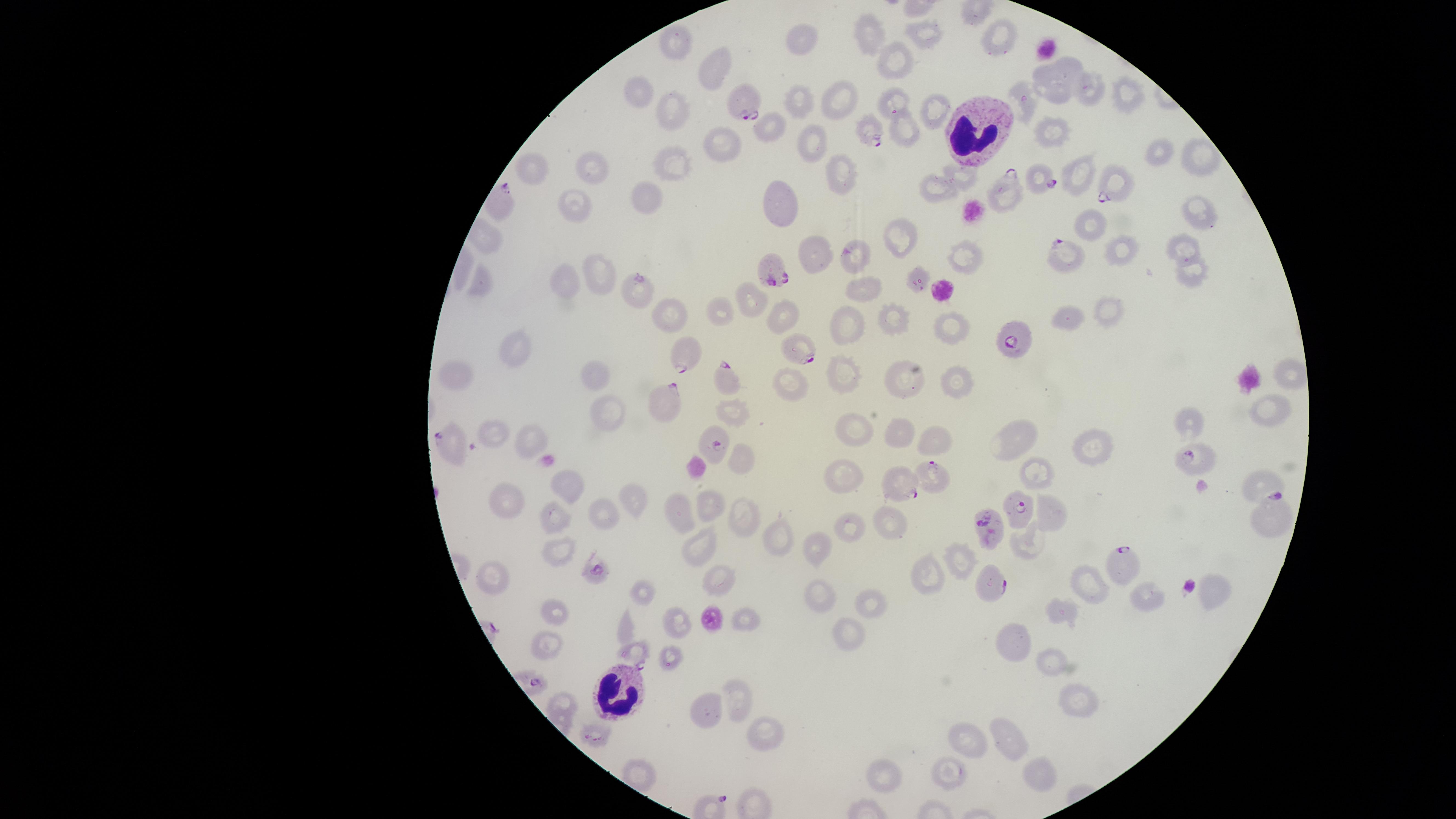

{
  "image_size": "1456×819 pixels",
  "presence": "malaria parasites identified",
  "parasitized_red_blood_cells": "approximate marker points as {x, y} in pixels: {745, 99}, {894, 100}, {870, 127}, {1040, 176}, {1118, 182}, {1002, 188}, {1060, 253}, {856, 256}, {776, 271}, {640, 293}, {1015, 335}, {801, 348}, {684, 351}, {726, 377}, {666, 396}, {714, 440}, {453, 441}, {1193, 459}, {930, 475}, {898, 485}, {1021, 509}, {1271, 514}, {994, 525}, {1127, 562}, {596, 570}, {990, 581}, {633, 652}",
  "uninfected_red_blood_cells": "approximate marker points as {x, y} in pixels: {927, 33}, {874, 35}, {998, 38}, {675, 44}, {801, 47}, {899, 59}, {710, 66}, {1069, 67}, {1049, 87}, {1090, 90}, {641, 94}, {1130, 94}, {836, 98}, {799, 100}, {1023, 104}, {678, 112}, {935, 112}, {768, 124}, {1051, 128}, {902, 135}, {812, 141}, {720, 142}, {1155, 155}, {674, 162}, {597, 170}, {529, 171}, {958, 174}, {837, 175}, {1073, 183}, {940, 189}, {646, 198}, {782, 202}, {1195, 202}, {577, 205}, {1097, 225}, {901, 235}, {1186, 243}, {819, 253}, {1126, 253}, {967, 261}, {1195, 266}, {596, 268}, {568, 274}, {923, 277}, {485, 285}, {861, 291}, {751, 303}, {722, 310}, {1104, 310}, {788, 312}, {1069, 318}, {670, 319}, {902, 321}, {848, 322}, {948, 325}, {516, 344}, {452, 369}, {596, 370}, {840, 373}, {911, 375}, {1289, 379}, {799, 381}, {954, 382}, {737, 406}, {605, 408}, {1272, 412}, {1186, 421}, {846, 423}, {896, 430}, {494, 434}, {1021, 438}, {530, 439}, {931, 440}, {1095, 451}, {742, 459}, {1035, 474}, {841, 478}, {1258, 482}, {573, 487}, {634, 497}, {509, 506}, {709, 508}, {1051, 513}, {605, 516}, {683, 516}, {738, 519}, {552, 520}, {887, 523}, {847, 527}, {778, 540}, {1024, 544}, {695, 546}, {558, 550}, {817, 550}, {962, 560}, {924, 571}, {497, 576}, {719, 583}, {1086, 585}, {639, 591}, {1211, 591}, {818, 596}, {1149, 597}, {866, 603}, {1062, 610}, {557, 615}, {743, 615}, {674, 621}, {840, 635}, {1018, 640}, {541, 645}, {670, 657}, {1056, 660}, {734, 697}, {562, 701}, {1076, 701}, {707, 709}, {762, 731}, {1012, 736}, {972, 742}, {946, 775}, {893, 777}, {1035, 777}",
  "field_of_view": "single",
  "preparation": "thin blood smear",
  "visible_region": "circular",
  "white_blood_cells": "approximate marker points as {x, y} in pixels: {980, 131}, {614, 696}",
  "stain": "Giemsa",
  "species": "Plasmodium falciparum",
  "capture": "smartphone photograph through the microscope eyepiece"
}